Assess for Plasmodium parasites.
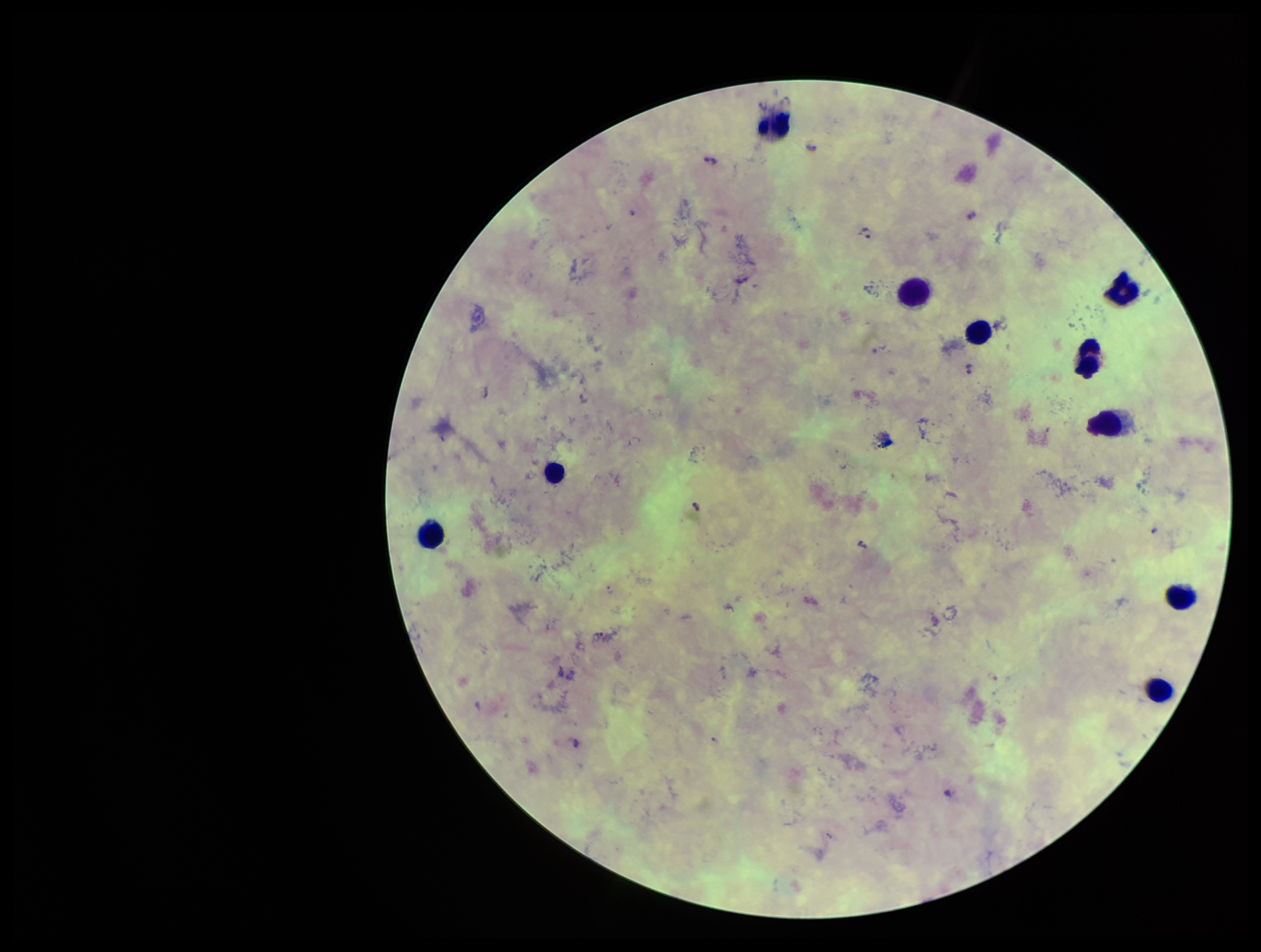
Detected.

Patient malaria status: positive. Smartphone photograph taken through the eyepiece of a microscope. Leukocyte count: 10. Image is 1261×952 pixels. Preparation: thick blood smear. Giemsa stain. Parasite count: 4. One field from this slide. Species reported for this patient: Plasmodium falciparum.